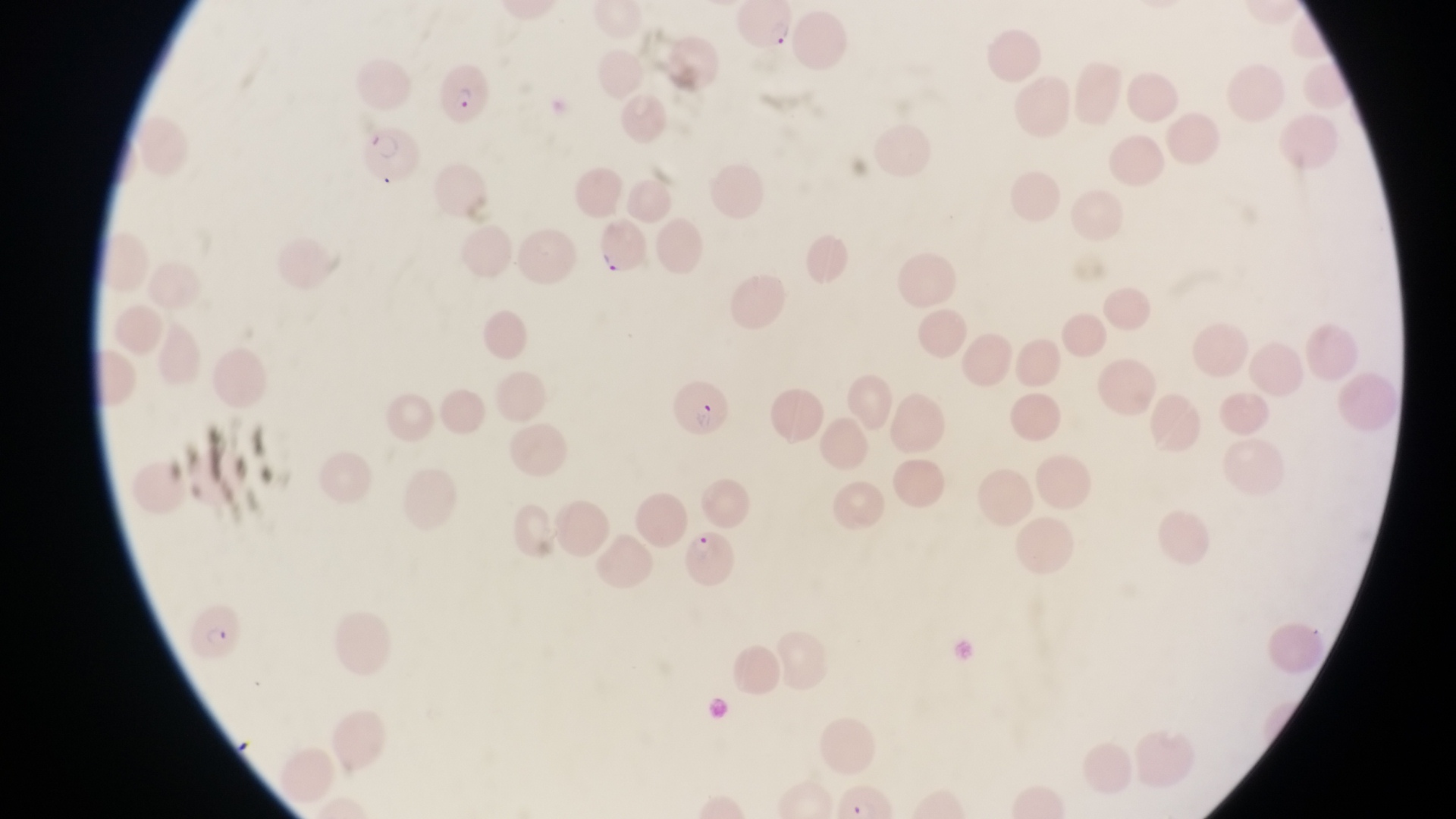

Approximate bounding boxes as [left, top, right, bottom] in pixels. Parasitised red blood cell locations: [734, 2, 793, 50], [442, 61, 494, 130], [362, 121, 421, 187], [597, 218, 650, 282], [667, 369, 736, 440], [682, 528, 737, 587], [191, 600, 246, 663]. Thin blood smear. Collected in Uganda. Image is 1456×819 pixels. One field of view. At a magnification of 1000x. Photographed through the eyepiece of an Olympus CX-23 microscope with a smartphone camera.